Classify this cell by malaria status.
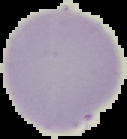

It is uninfected.

image type = cell region segmented out of the field of view; surrounding area masked to black
preparation = thin blood smear
image size = 127×139 pixels